Classify this cell by malaria status.
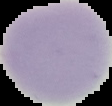
Uninfected.

Summary:
  - Preparation: thin blood film
  - Image size: 112×106 pixels
  - Image type: cell region segmented out of the field of view; surrounding area masked to black